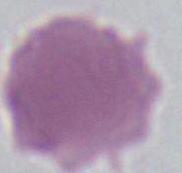

Captured at 1000x magnification. An erythrocyte is shown. Micrograph.